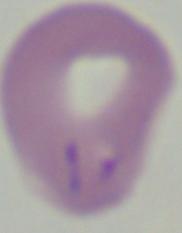
identification: Babesia
magnification: 1000x
modality: micrograph